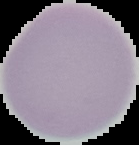 Image is 139×145 pixels. Result: negative for malaria parasites. Cell region segmented out of the field of view; the surrounding area is masked to black. From a thin blood film.